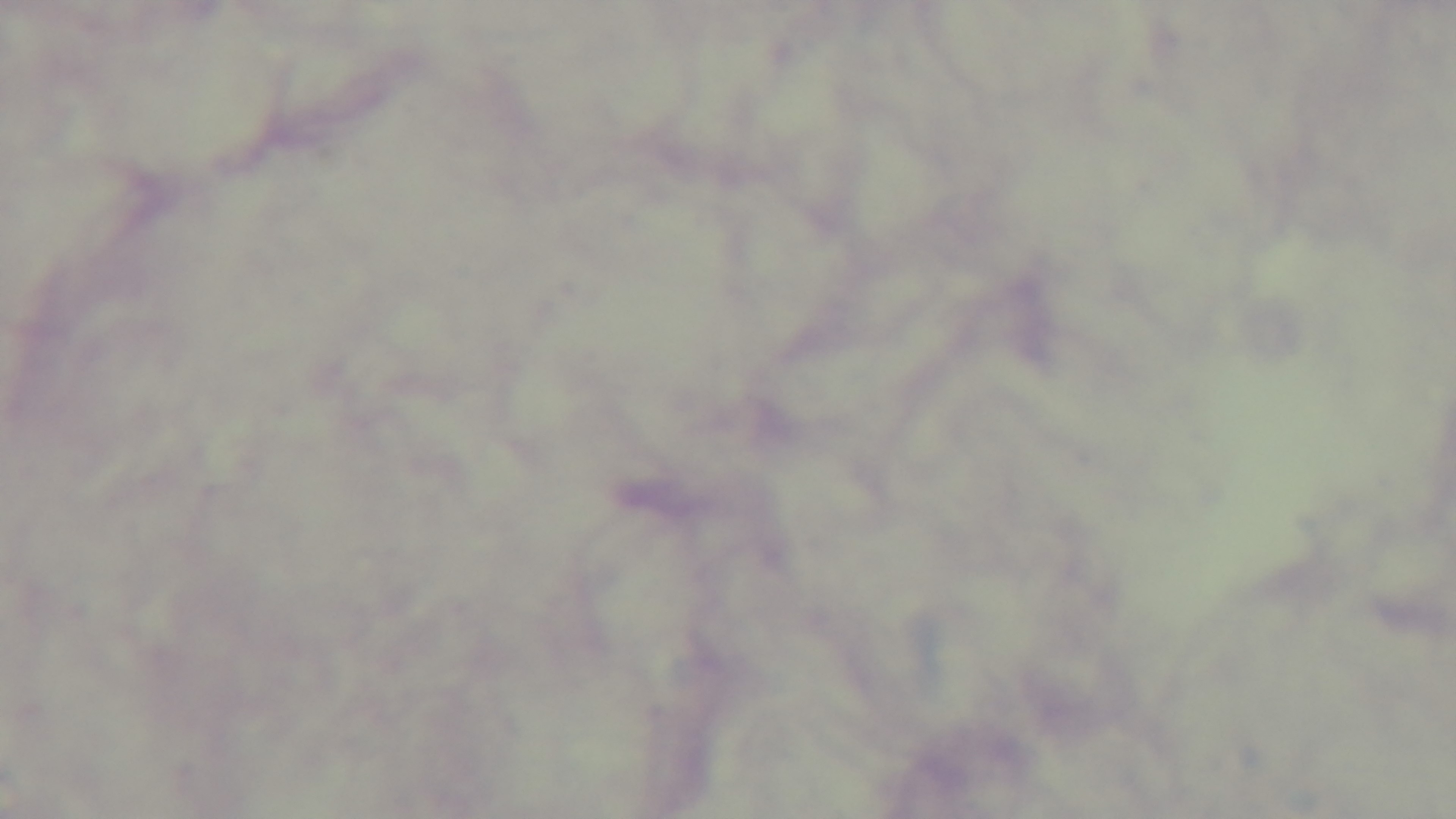

Photomicrograph. 100x oil-immersion objective. Giemsa-stained. Single field of view. Captured with a mounted 4K digital camera. Preparation: thick. Malaria status: uninfected.